Locate every Plasmodium vivax-infected red blood cell.
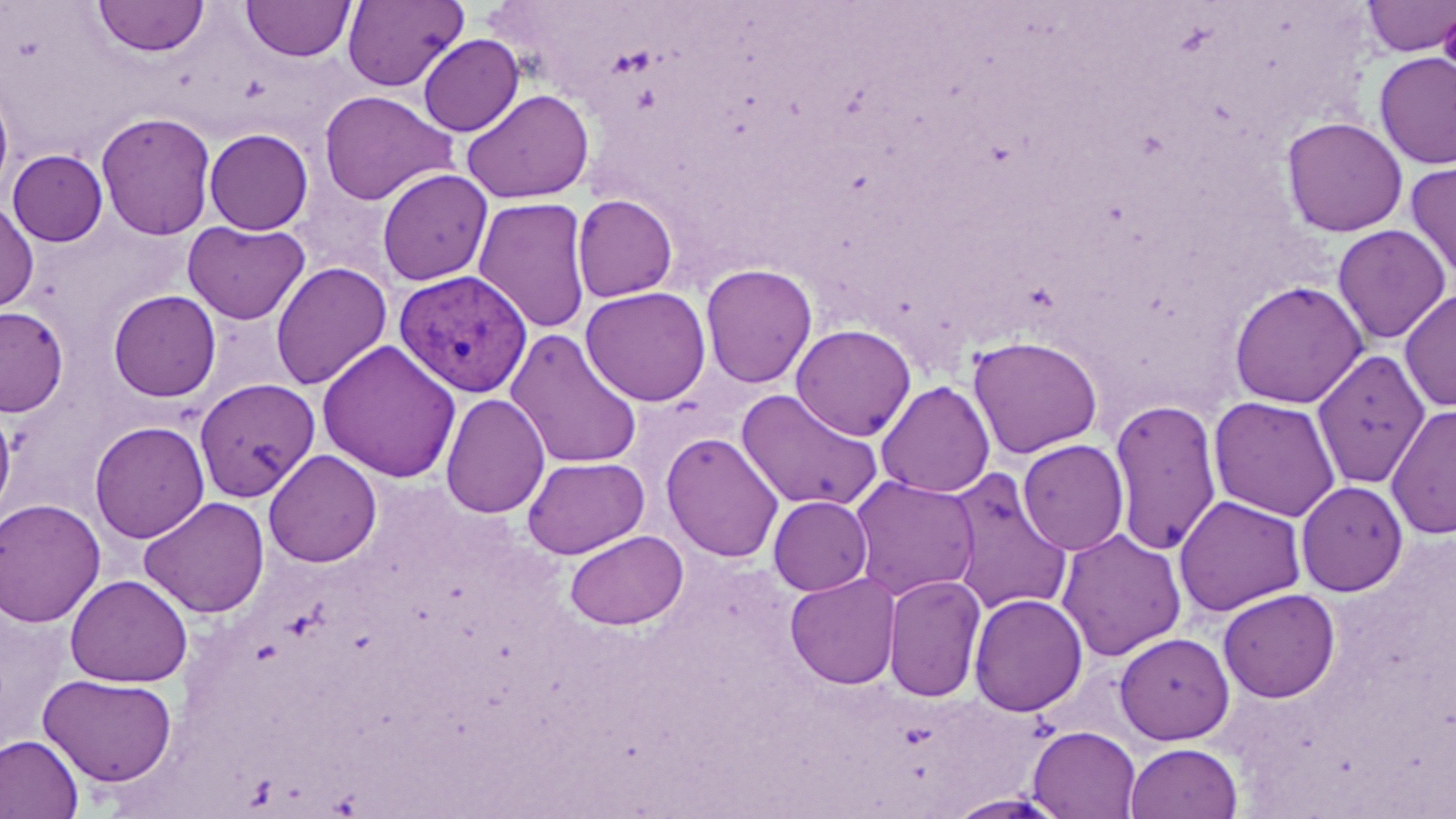

Approximate bounding boxes as (x1,y1)-(x2,y2) corner pairs in pixels.
Plasmodium vivax-infected red blood cells: (394,270)-(532,397).

Summary:
  - Uninfected red blood cell locations: (92,0)-(210,57), (341,0)-(469,92), (1361,0)-(1456,57), (241,1)-(356,62), (1437,5)-(1456,81), (418,34)-(524,136), (1374,51)-(1456,171), (0,79)-(14,205), (462,88)-(594,204), (318,90)-(458,206), (95,111)-(217,240), (1281,115)-(1408,237), (204,128)-(314,235), (7,149)-(108,246), (1405,159)-(1456,282), (377,169)-(492,286), (572,194)-(678,302), (473,196)-(592,335), (0,199)-(39,313), (182,220)-(310,324), (1332,224)-(1452,345), (270,261)-(392,390), (700,262)-(818,389), (1228,279)-(1368,409), (580,286)-(711,406), (1399,288)-(1456,413), (108,289)-(221,402), (0,306)-(69,417), (791,324)-(916,441), (505,329)-(643,470), (967,334)-(1103,459), (317,340)-(461,483), (1311,349)-(1430,489), (194,378)-(320,502), (875,380)-(995,498), (736,388)-(884,511), (440,393)-(550,519), (1208,395)-(1341,522), (1108,398)-(1223,556), (0,400)-(16,522), (1386,402)-(1456,540), (89,420)-(210,543), (661,432)-(784,563), (1017,439)-(1129,556), (264,449)-(382,567), (522,456)-(649,558), (943,468)-(1074,616), (848,475)-(980,601), (1296,480)-(1407,596), (1173,494)-(1307,616), (768,495)-(873,595), (138,496)-(270,619), (0,498)-(106,627), (1056,528)-(1187,660), (564,529)-(688,630), (785,572)-(901,690), (882,573)-(987,702), (65,574)-(193,687), (1217,588)-(1341,702), (968,592)-(1088,717), (1114,632)-(1235,745), (38,673)-(178,787), (1027,726)-(1141,818), (0,733)-(84,819), (1125,742)-(1243,819), (944,792)-(1070,818)
  - Slide-level diagnosis: Plasmodium vivax
  - Image size: 1456×819 pixels
  - Modality: light microscopy
  - Preparation: thin blood smear
  - Field of view: single
  - Stain: May-Grünwald-Giemsa
  - Magnification: 1000x